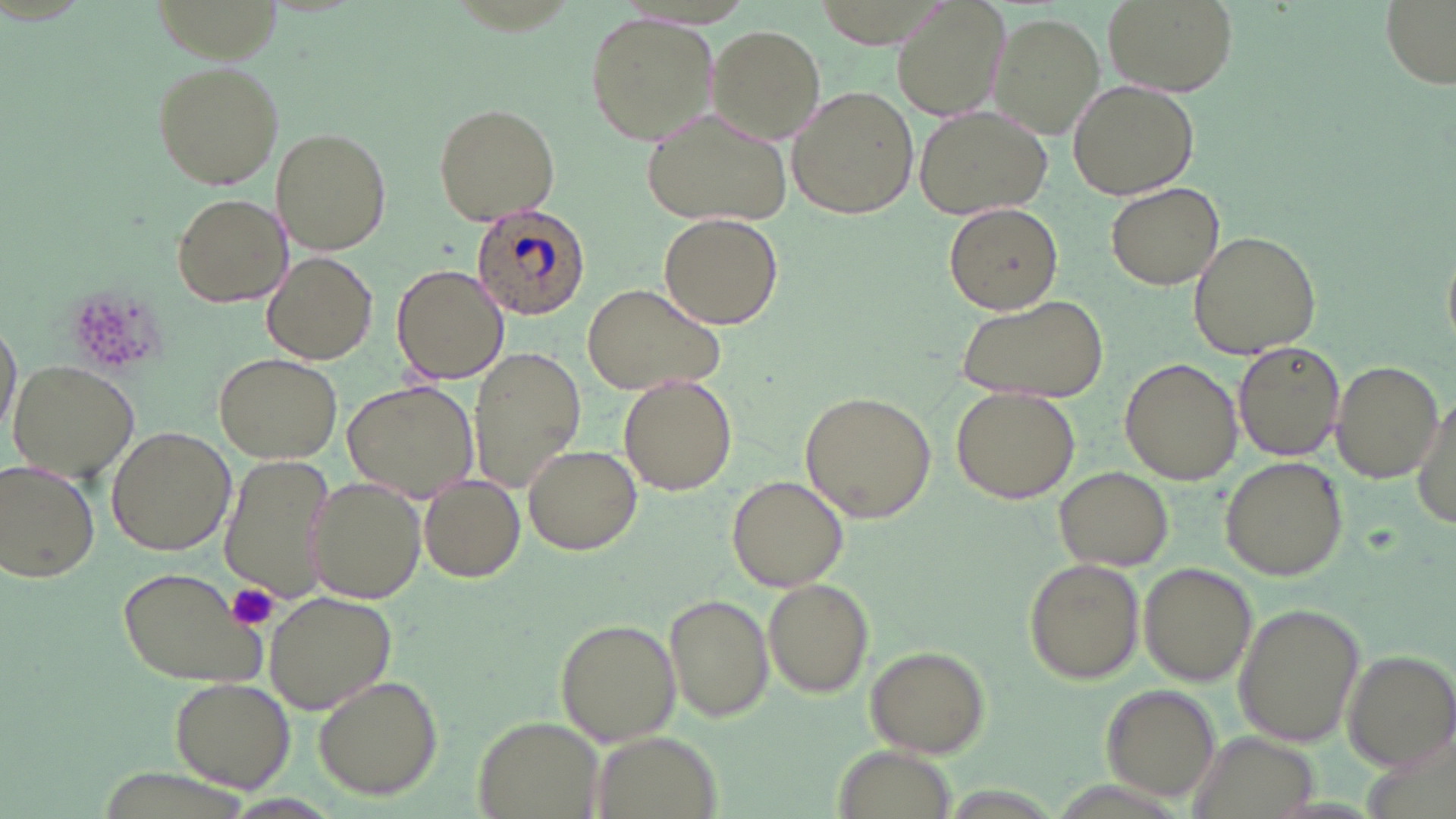

{
  "slide_level_diagnosis": "Plasmodium ovale",
  "uninfected_red_blood_cell_locations": "approximate bounding boxes as (x1,y1)-(x2,y2) corner pairs in pixels: (889,0)-(1013,122), (1104,0)-(1236,97), (1377,0)-(1454,87), (584,13)-(719,143), (989,14)-(1104,139), (708,25)-(825,142), (152,61)-(285,189), (1067,80)-(1200,201), (786,86)-(918,220), (432,102)-(562,226), (913,105)-(1053,217), (643,107)-(795,226), (272,129)-(391,253), (1106,181)-(1225,290), (171,193)-(291,309), (943,201)-(1064,315), (658,212)-(783,329), (1187,230)-(1322,360), (263,251)-(378,364), (391,262)-(510,387), (580,283)-(727,397), (953,291)-(1110,403), (1,317)-(19,446), (1233,341)-(1346,463), (468,348)-(587,494), (214,353)-(343,463), (1330,358)-(1442,482), (1119,359)-(1241,483), (7,361)-(141,483), (619,373)-(737,497), (341,377)-(479,502), (949,388)-(1080,503), (799,391)-(936,522), (1407,391)-(1454,531), (106,425)-(235,555), (523,444)-(643,554), (218,456)-(339,607), (1219,456)-(1348,581), (2,459)-(102,584), (1055,467)-(1173,571), (420,474)-(526,582), (727,474)-(849,591), (305,478)-(427,604), (1025,559)-(1145,683), (1137,563)-(1257,690), (117,566)-(268,689), (763,577)-(874,697), (264,590)-(397,716), (666,595)-(773,721), (1233,602)-(1366,748), (554,618)-(683,747), (866,646)-(990,759), (1344,651)-(1456,771), (169,677)-(295,792), (313,677)-(442,801), (1101,685)-(1223,803), (472,715)-(607,819), (588,729)-(718,818), (1189,731)-(1318,816), (832,745)-(962,817)",
  "modality": "optical microscopy",
  "plasmodium_ovale_infected_red_blood_cell_locations": "approximate bounding boxes as (x1,y1)-(x2,y2) corner pairs in pixels: (474,206)-(587,321)",
  "preparation": "thin blood film",
  "platelet_locations": "approximate bounding boxes as (x1,y1)-(x2,y2) corner pairs in pixels: (224,583)-(281,631)",
  "field_of_view": "single",
  "magnification": "1000x",
  "stain": "May-Grünwald-Giemsa",
  "image_size": "1456×819 pixels"
}